State which parasite is depicted.
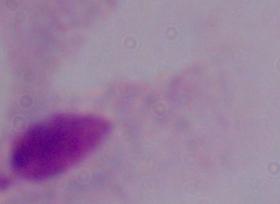
A trichomonad.

Summary:
  - Magnification: 1000x
  - Modality: photomicrograph